Point out Plasmodium parasites and leukocytes.
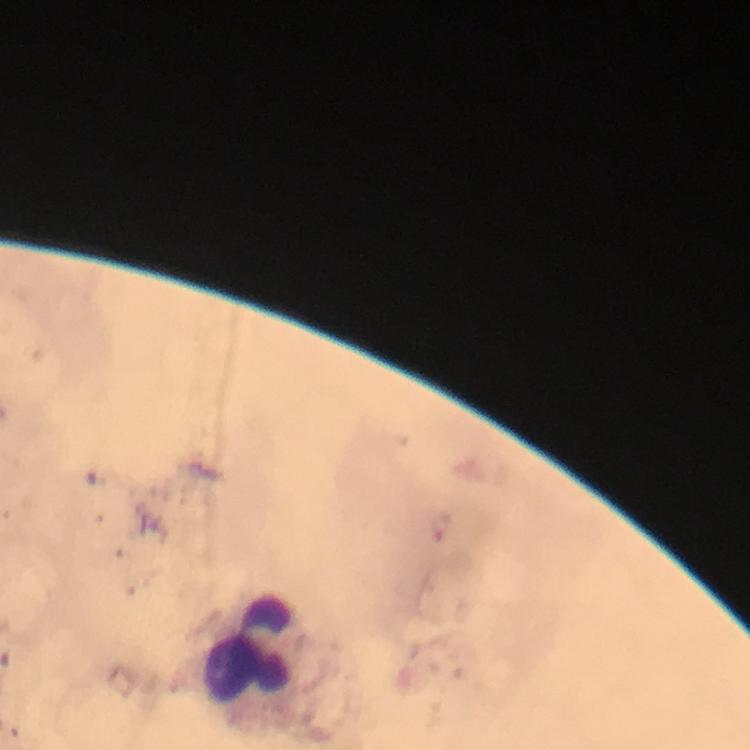
No Plasmodium parasites seen.
Approximate centers as {x, y} in pixels.
Leukocytes: {250, 646}.

{
  "context": "from a diagnostic examination for malaria",
  "stain": "Giemsa",
  "immersion_oil": "used",
  "magnification": "100x",
  "cropped_from": "a single field of view",
  "capture": "smartphone camera through the microscope",
  "preparation": "thick blood film",
  "image_size": "750×750 pixels"
}